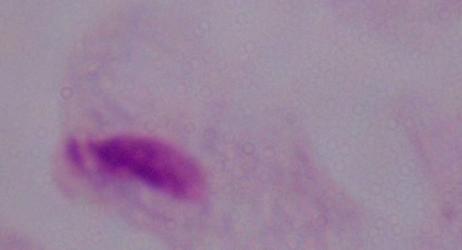

Micrograph. A trichomonad is seen. 1000x magnification.